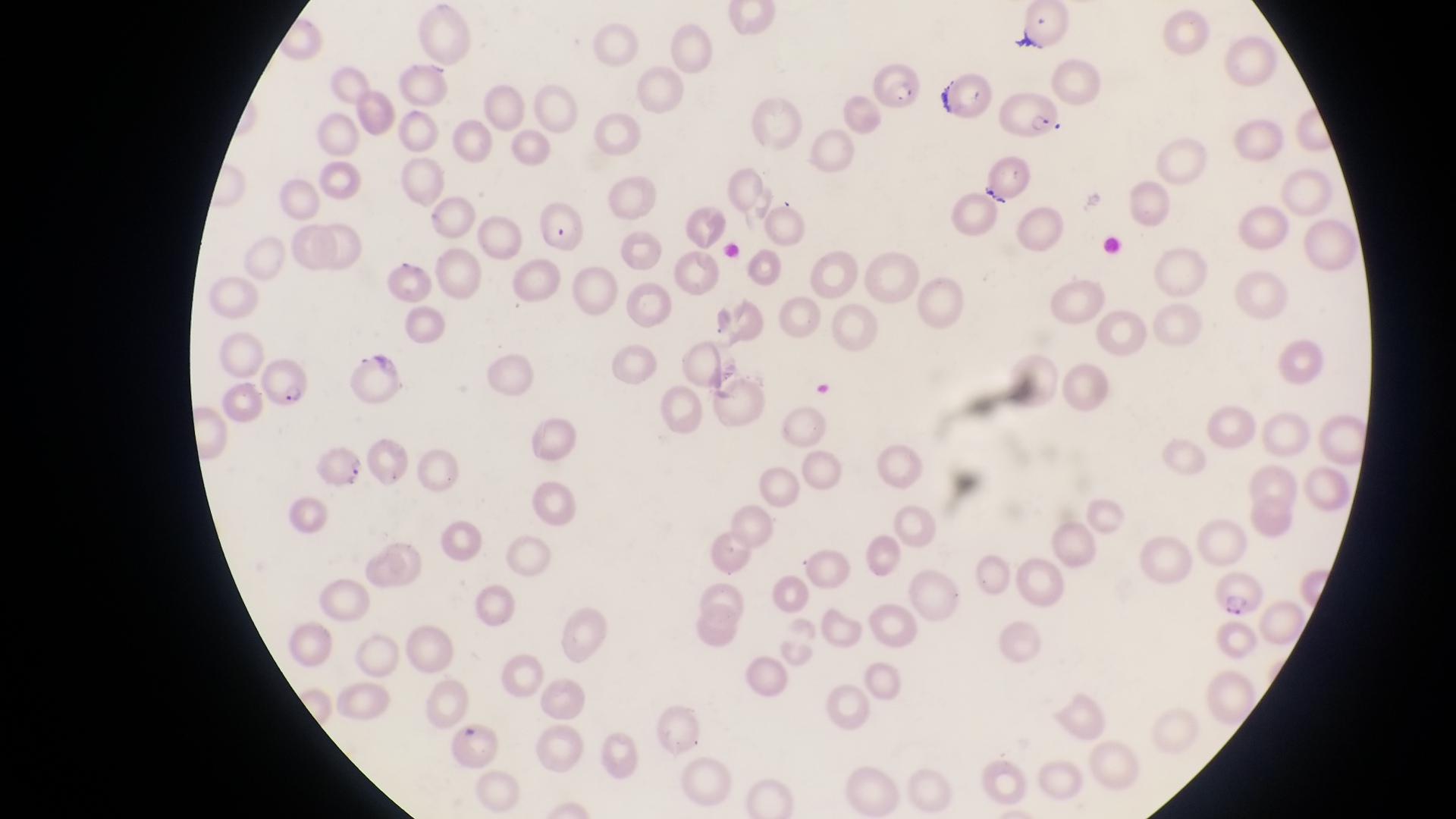

field of view = single
capture = smartphone photograph through the eyepiece of an Olympus CX-23 microscope
magnification = 1000x
image size = 1456×819 pixels
country = Uganda
preparation = thin blood film
parasitised red blood cell locations = approximate bounding boxes as left top right bottom in pixels: 868 58 931 114; 999 87 1065 143; 532 198 591 253; 258 357 311 415; 310 438 364 491